Comment on the morphology of the erythrocytes.
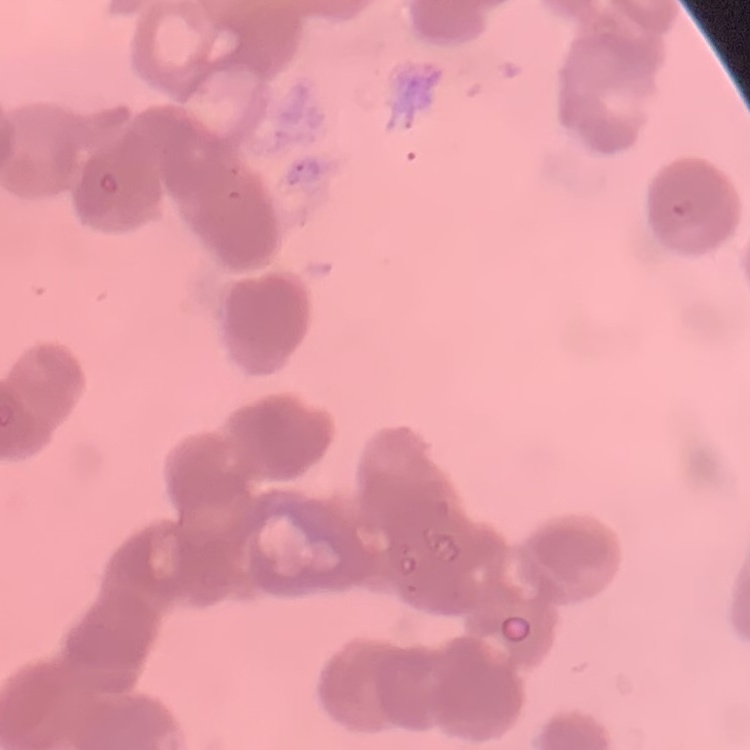
Rouleaux formation.

Thin peripheral smear. Field's or Giemsa stain. Square crop of a larger photomicrograph.